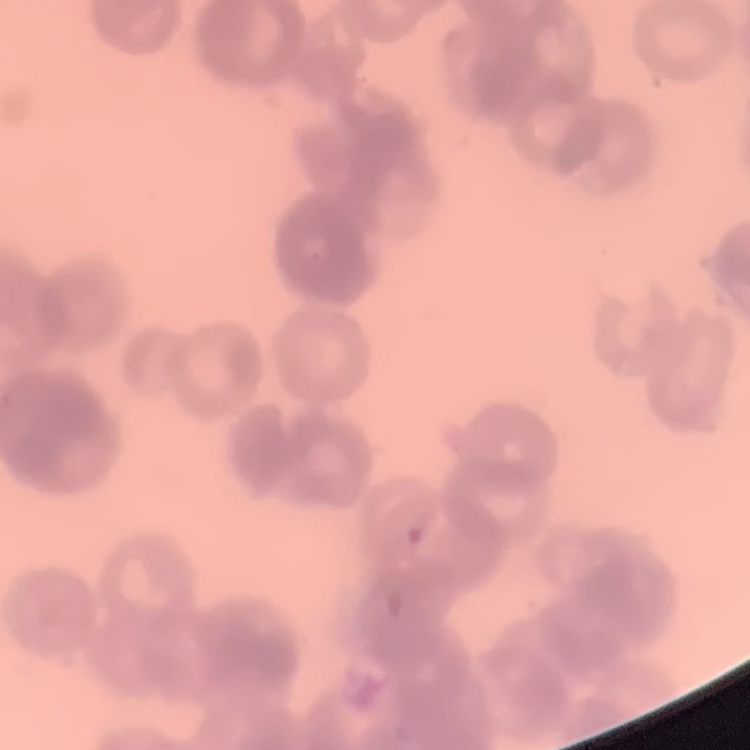
red blood cell morphology = rouleaux formation
preparation = thin blood smear
image type = square crop of a larger photomicrograph
stain = Field's or Giemsa